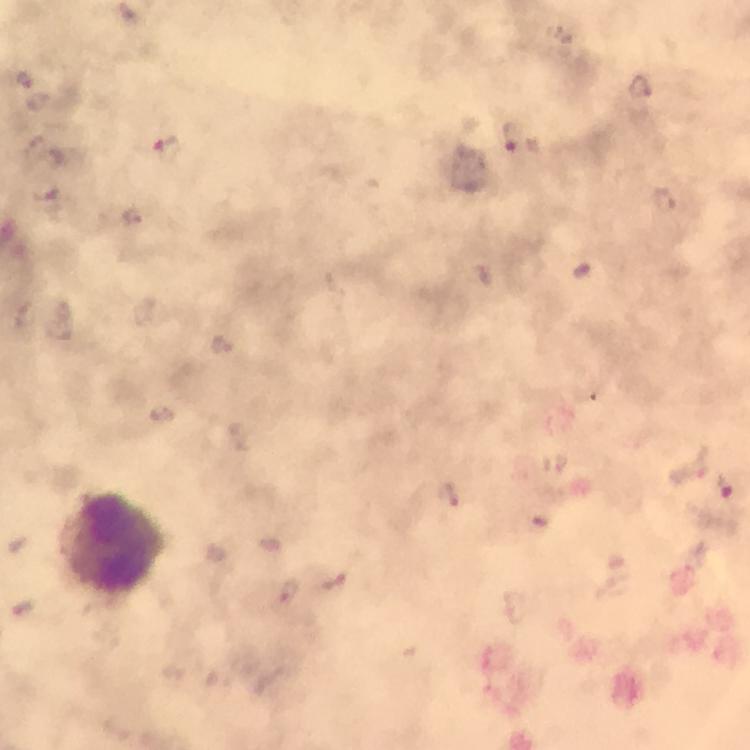
{
  "magnification": "100x",
  "cropped_from": "one field of view",
  "leukocyte_locations": "approximate object centers, in pixels from the top-left corner: (x=113, y=543)",
  "image_size": "750×750 pixels",
  "capture": "smartphone photograph through a microscope",
  "immersion_oil": "applied",
  "plasmodium_parasite_locations": "approximate object centers, in pixels from the top-left corner: (x=25, y=80), (x=641, y=86), (x=513, y=138), (x=37, y=151), (x=165, y=151), (x=662, y=199), (x=135, y=216), (x=690, y=466), (x=725, y=488), (x=449, y=495), (x=335, y=580), (x=287, y=593)",
  "context": "from a malaria diagnostic workup",
  "preparation": "thick blood film",
  "stain": "Giemsa"
}